Classify this cell by malaria status.
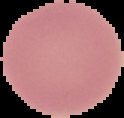

Uninfected.

{
  "image_size": "124×118 pixels",
  "preparation": "thin blood film",
  "image_type": "segmented cell region on a black background"
}